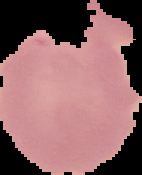

Summary:
  - Result: Plasmodium parasites identified
  - Preparation: thin blood film
  - Image size: 142×175 pixels
  - Image type: segmented cell region on a black background